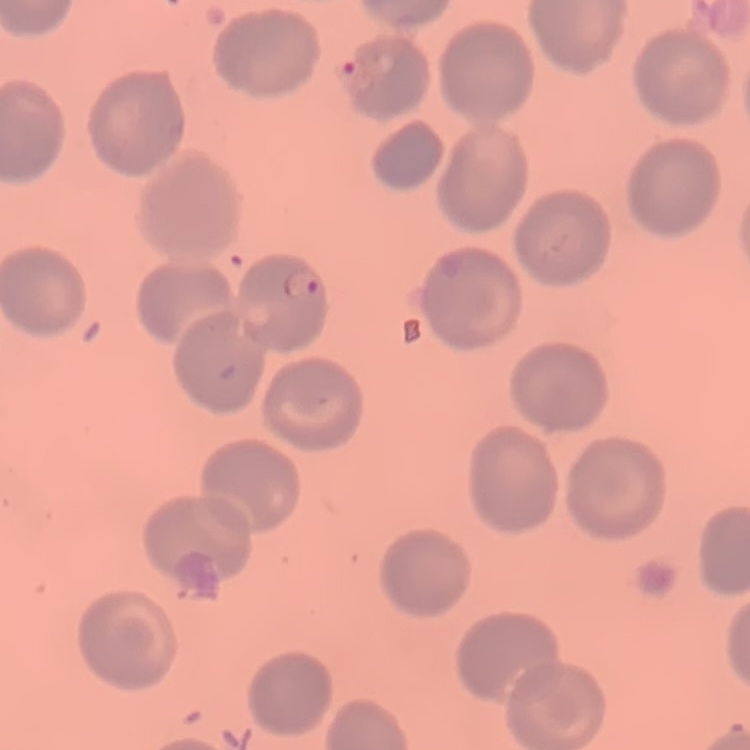

erythrocyte_morphology: no rouleaux formation
preparation: thin blood film
stain: Field's or Giemsa
image_type: square crop of a larger photomicrograph